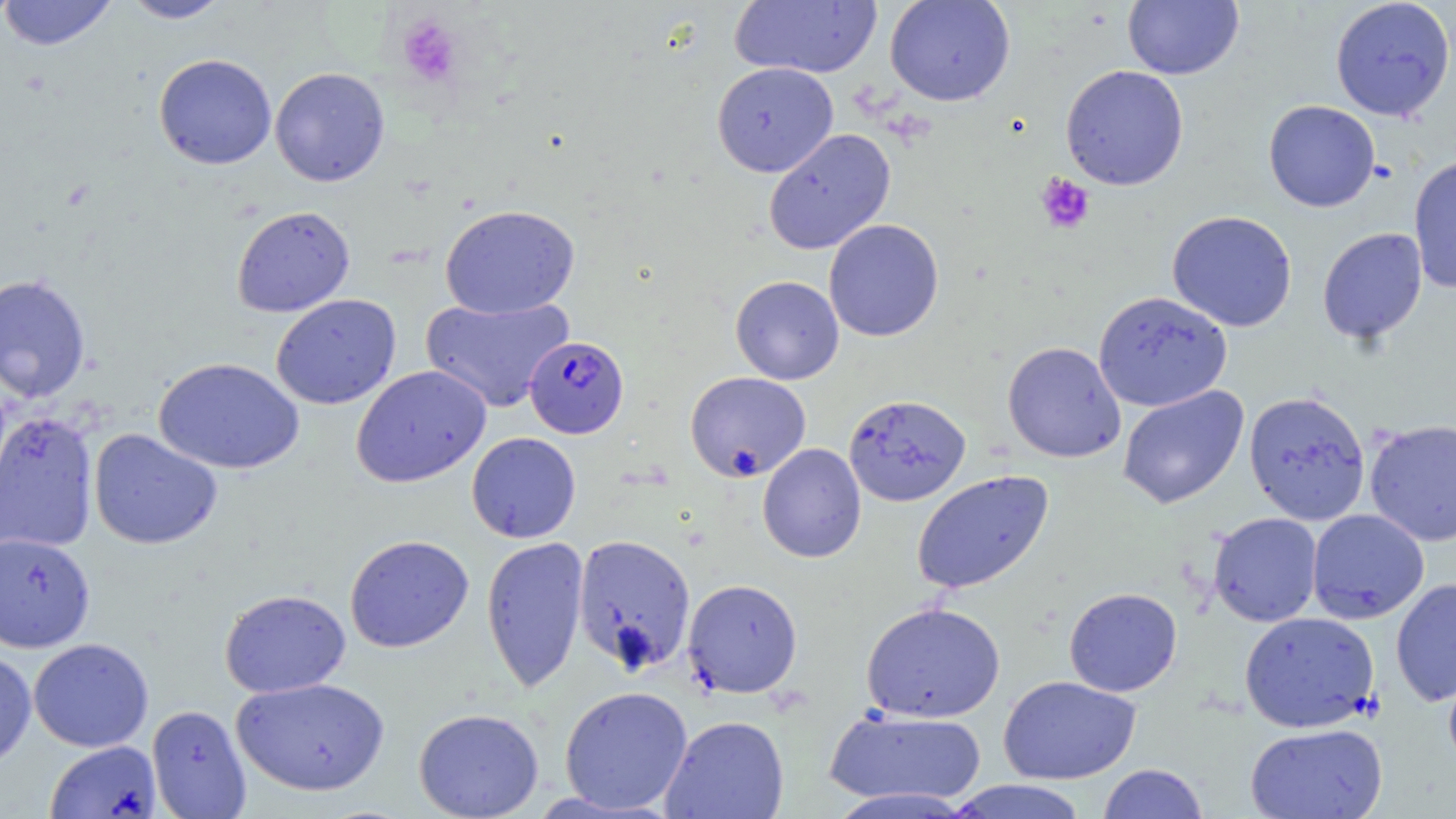 Approximate bounding boxes as [x1, y1, x2, y2] in pixels. Plasmodium falciparum-infected red blood cell locations: [524, 335, 629, 439]. Uninfected red blood cell locations: [0, 0, 118, 51], [121, 0, 234, 24], [884, 0, 1016, 106], [1122, 0, 1244, 80], [1330, 0, 1454, 122], [729, 1, 882, 79], [153, 53, 277, 169], [711, 62, 838, 177], [1060, 65, 1189, 190], [270, 67, 390, 187], [1263, 100, 1380, 212], [763, 128, 896, 255], [1408, 155, 1456, 293], [439, 203, 580, 318], [231, 205, 355, 317], [1166, 210, 1298, 332], [823, 219, 945, 342], [1317, 227, 1427, 345], [0, 274, 91, 403], [730, 275, 844, 384], [1093, 291, 1232, 412], [271, 294, 401, 410], [420, 296, 574, 413], [1002, 341, 1126, 463], [153, 356, 305, 474], [350, 364, 492, 488], [684, 371, 811, 482], [1117, 385, 1249, 510], [1243, 391, 1371, 525], [844, 394, 971, 507], [0, 411, 99, 554], [1364, 419, 1456, 547], [88, 428, 223, 550], [466, 432, 581, 543], [757, 443, 867, 563], [911, 470, 1054, 595], [1306, 509, 1430, 623], [1207, 512, 1323, 627], [0, 532, 96, 652], [572, 533, 697, 675], [344, 534, 474, 653], [481, 536, 589, 693], [1390, 577, 1456, 706], [682, 578, 803, 698], [1064, 587, 1182, 697], [219, 588, 351, 697], [860, 601, 1006, 723], [1239, 611, 1380, 733], [28, 638, 154, 752], [0, 649, 36, 770], [1442, 656, 1456, 775], [998, 675, 1141, 784], [231, 677, 390, 796], [559, 685, 693, 814], [146, 704, 252, 819], [824, 706, 988, 807], [413, 707, 544, 819], [660, 715, 790, 819], [1244, 723, 1388, 818], [44, 740, 161, 819], [1097, 763, 1209, 819], [944, 779, 1091, 819], [824, 787, 977, 817]. Platelet locations: [396, 13, 464, 87], [1035, 173, 1095, 234]. Slide-level diagnosis: Plasmodium falciparum. 1000x magnification. May-Grünwald-Giemsa-stained preparation. Optical microscopy. Thin blood smear. Single field of view. Image is 1456×819 pixels.